Identify the preparation type.
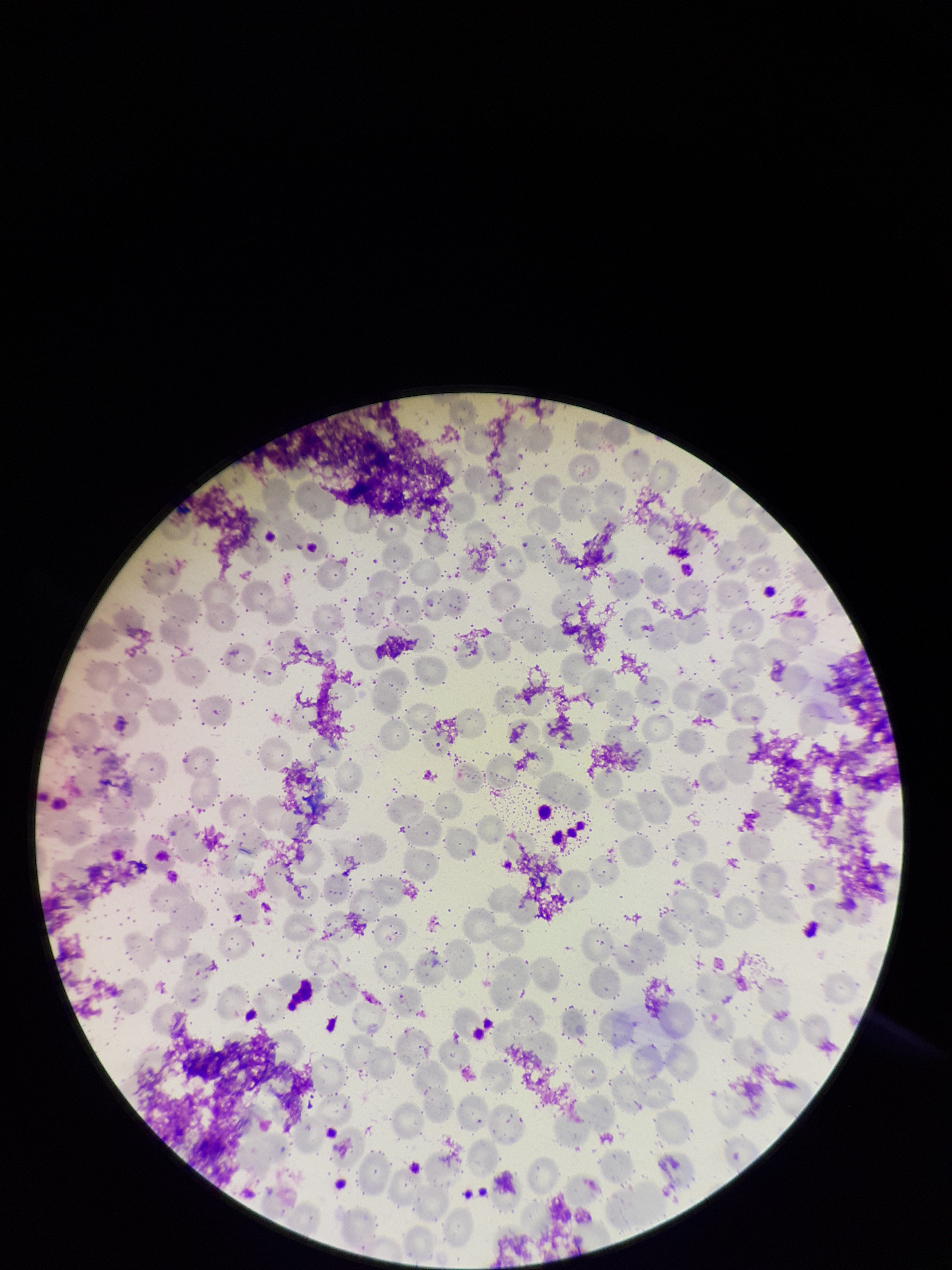

A thin smear.

Summary:
  - Parasitized red blood cell count: 0
  - Image size: 952×1270 pixels
  - Patient malaria status: negative
  - Field of view: one from this slide
  - Red blood cell count: 254
  - Parasitized red blood cells: none detected
  - Capture: smartphone photograph through the microscope eyepiece
  - Stain: Giemsa